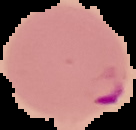
image size = 136×130 pixels
preparation = thin blood smear
result = malaria parasites identified
image type = segmented cell region on a black background